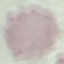

malaria status = uninfected
preparation = thin blood smear
stain = Giemsa
image type = cell patch, automatically extracted from a larger field of view and resized to 64 × 64 pixels
capture = smartphone through the microscope eyepiece